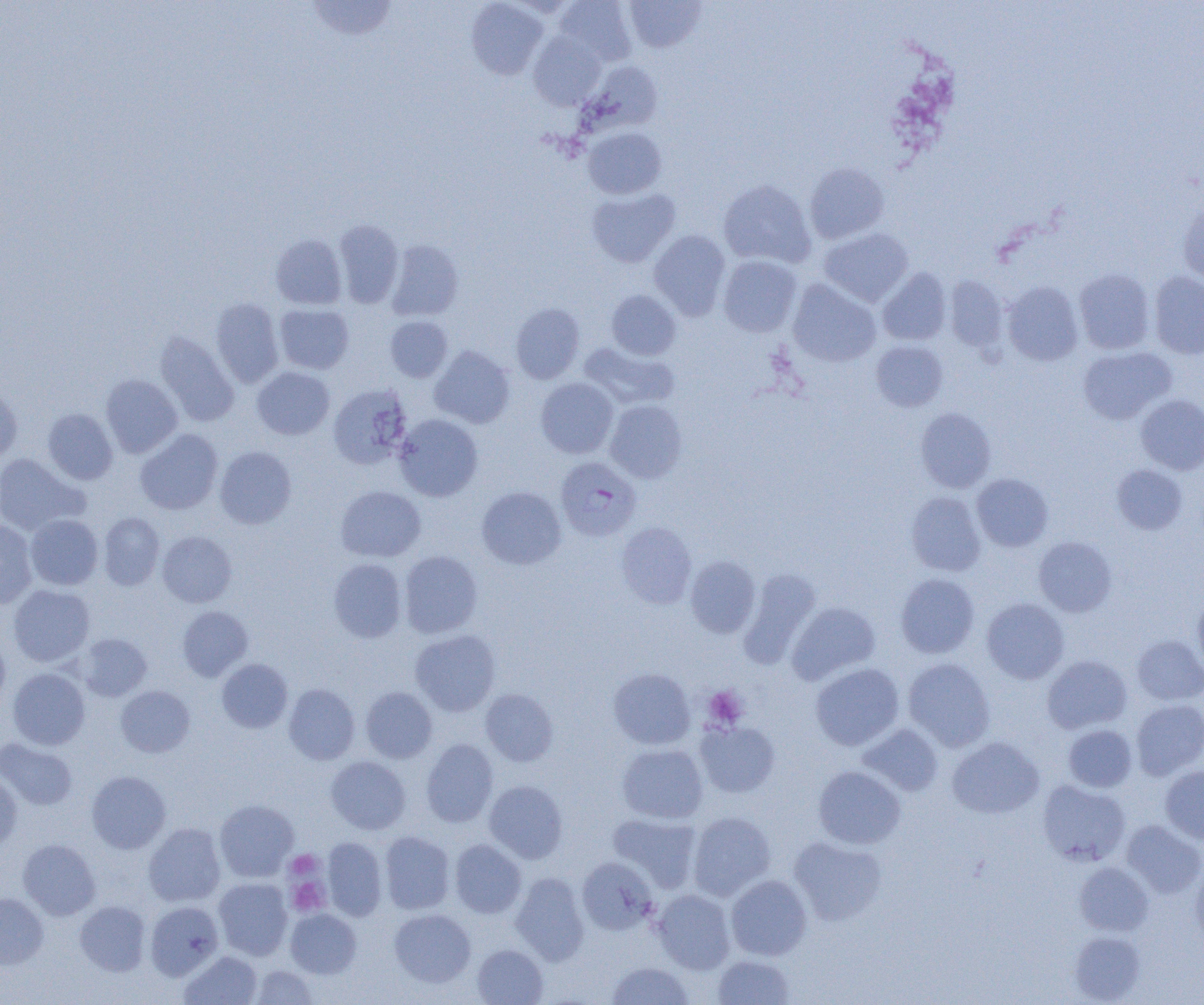

Summary:
  - Coordinate format: approximate bounding boxes as [x1, y1, x2, y2] in pixels
  - Plasmodium falciparum-infected red blood cell locations: [555, 456, 642, 542]
  - Platelet locations: [703, 686, 748, 729], [286, 850, 322, 879], [286, 873, 330, 916]
  - Uninfected red blood cell locations: [305, 0, 399, 41], [466, 0, 548, 80], [554, 0, 636, 66], [625, 1, 706, 52], [528, 32, 606, 110], [584, 60, 663, 133], [583, 127, 666, 199], [804, 162, 889, 244], [718, 180, 816, 268], [586, 188, 680, 267], [1178, 202, 1204, 284], [333, 219, 404, 308], [819, 228, 913, 307], [649, 229, 730, 320], [270, 234, 347, 309], [386, 239, 463, 320], [718, 255, 802, 337], [877, 268, 951, 345], [1074, 269, 1154, 354], [1149, 271, 1204, 359], [945, 275, 1008, 353], [788, 279, 881, 367], [1002, 281, 1083, 366], [606, 290, 681, 360], [210, 298, 284, 387], [510, 302, 584, 384], [274, 304, 354, 374], [385, 316, 452, 382], [154, 331, 239, 427], [870, 340, 947, 412], [578, 341, 679, 410], [429, 346, 515, 429], [1078, 346, 1176, 424], [252, 367, 334, 440], [100, 374, 182, 458], [536, 378, 619, 458], [0, 384, 22, 463], [328, 384, 412, 469], [1136, 395, 1204, 475], [605, 400, 687, 483], [42, 408, 118, 485], [915, 408, 997, 492], [394, 414, 483, 501], [135, 429, 222, 515], [215, 446, 296, 529], [0, 454, 88, 534], [1111, 465, 1188, 535], [971, 473, 1054, 552], [335, 485, 426, 562], [477, 486, 566, 570], [906, 491, 986, 576], [98, 512, 165, 590], [25, 514, 103, 590], [0, 520, 38, 608], [616, 521, 697, 609], [157, 531, 237, 608], [1034, 536, 1117, 617], [399, 550, 483, 638], [685, 555, 760, 638], [328, 558, 407, 642], [738, 569, 821, 669], [895, 573, 980, 658], [8, 584, 95, 667], [1192, 594, 1204, 674], [982, 598, 1069, 684], [787, 601, 880, 684], [177, 606, 253, 681], [410, 629, 500, 716], [76, 633, 152, 701], [0, 634, 11, 712], [1132, 635, 1204, 705], [1042, 655, 1132, 734], [216, 658, 293, 733], [903, 658, 995, 751], [810, 662, 904, 751], [7, 668, 90, 750], [608, 668, 696, 749], [284, 684, 360, 764], [116, 685, 195, 757], [361, 686, 437, 763], [481, 689, 558, 766], [1131, 699, 1204, 779], [695, 720, 780, 798], [858, 723, 943, 796], [1063, 724, 1137, 792], [947, 736, 1044, 818], [0, 738, 78, 810], [421, 738, 499, 827], [616, 743, 708, 824], [325, 756, 410, 835], [813, 765, 906, 849], [1160, 765, 1204, 844], [86, 770, 171, 853], [0, 771, 22, 850], [484, 780, 568, 863], [1037, 780, 1130, 866], [214, 799, 298, 881], [688, 811, 776, 900], [607, 812, 702, 893], [1121, 820, 1204, 898], [144, 823, 225, 907], [380, 831, 455, 914], [789, 835, 887, 926], [322, 837, 387, 921], [18, 839, 101, 920], [450, 839, 526, 918], [577, 857, 658, 934], [1189, 861, 1204, 948], [1074, 862, 1154, 936], [511, 872, 590, 966], [726, 875, 812, 960], [214, 878, 292, 960], [653, 889, 735, 974], [0, 892, 49, 969], [75, 901, 150, 975], [145, 901, 223, 980], [389, 908, 476, 987], [285, 909, 361, 978], [1068, 930, 1146, 1004], [472, 944, 548, 1005], [179, 950, 262, 1005], [712, 954, 795, 1004], [605, 961, 694, 1005], [249, 965, 319, 1004]
  - Slide-level diagnosis: Plasmodium falciparum
  - Field of view: single
  - Modality: optical microscopy
  - Magnification: 1000x
  - Preparation: thin blood smear
  - Image size: 1204×1005 pixels